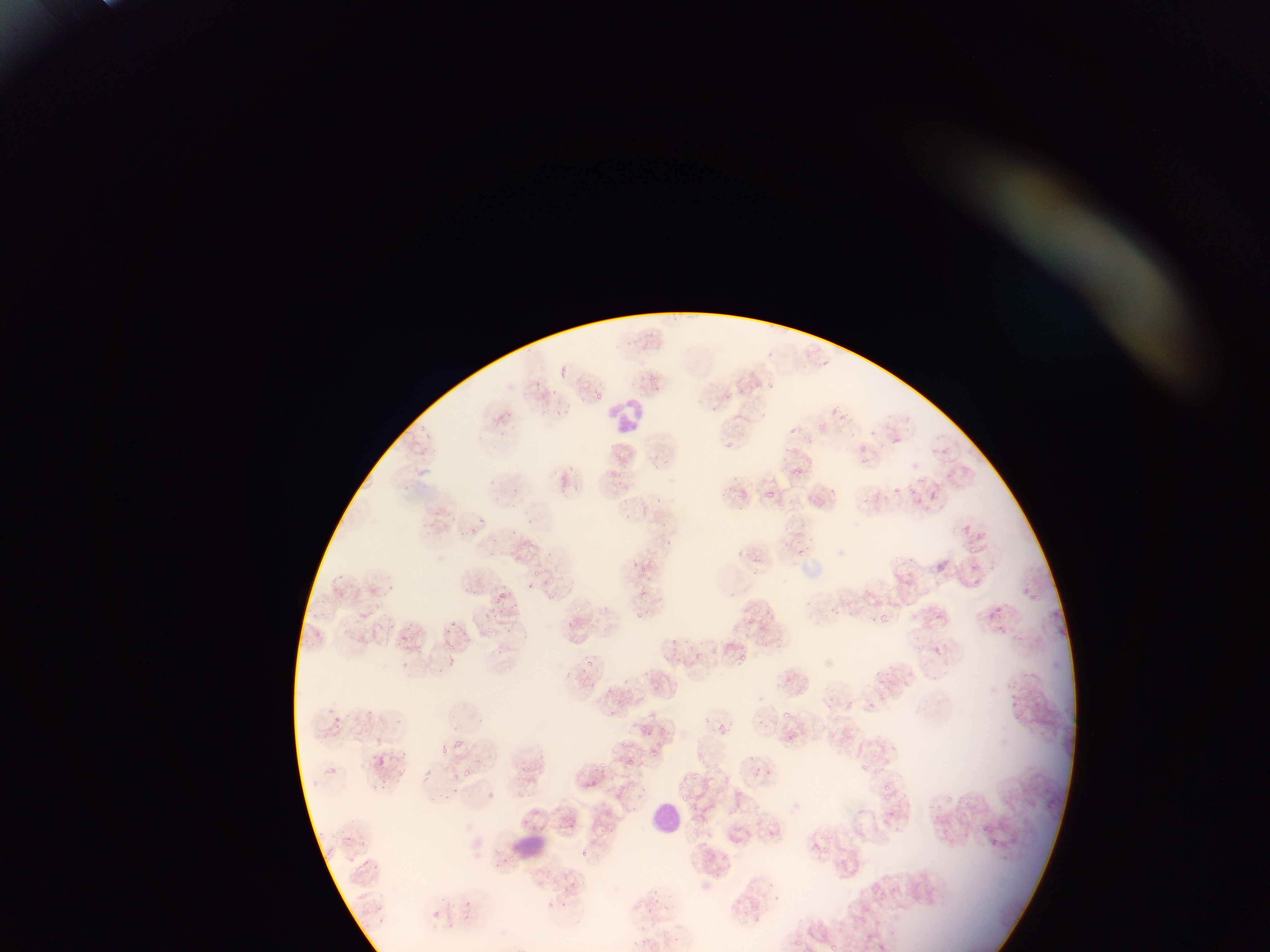
Plasmodium parasite locations = approximate bounding boxes as {left, top, right, bottom} in pixels: {639, 372, 656, 386}, {580, 387, 597, 407}, {543, 388, 570, 408}, {831, 407, 840, 415}, {553, 408, 571, 422}, {864, 423, 874, 436}, {788, 427, 798, 435}, {892, 434, 910, 453}, {852, 450, 880, 472}, {789, 462, 808, 486}, {764, 477, 778, 505}, {614, 479, 624, 490}, {893, 481, 905, 501}, {928, 486, 940, 502}, {653, 495, 673, 511}, {617, 507, 632, 526}, {477, 514, 486, 524}, {505, 528, 517, 540}, {661, 533, 669, 549}, {793, 542, 806, 560}, {918, 551, 957, 575}, {631, 558, 645, 573}, {336, 571, 350, 579}, {528, 577, 540, 593}, {454, 583, 474, 595}, {1017, 585, 1041, 599}, {638, 586, 645, 596}, {498, 589, 511, 605}, {825, 602, 837, 617}, {989, 605, 1005, 619}, {877, 609, 902, 623}, {631, 610, 654, 629}, {443, 615, 451, 625}, {738, 615, 752, 633}, {564, 618, 574, 630}, {436, 628, 448, 642}, {670, 636, 678, 642}, {727, 637, 747, 670}, {933, 647, 945, 655}, {447, 650, 457, 666}, {695, 650, 703, 670}, {587, 660, 594, 672}, {622, 675, 629, 687}, {864, 697, 876, 707}, {364, 702, 372, 712}, {320, 707, 342, 725}, {751, 715, 767, 734}, {640, 718, 655, 735}, {719, 718, 731, 735}, {372, 735, 386, 749}, {439, 744, 448, 754}, {648, 747, 657, 759}, {370, 753, 389, 768}, {584, 753, 607, 780}, {625, 754, 638, 772}, {747, 754, 757, 762}, {863, 763, 877, 775}, {462, 767, 472, 776}, {884, 782, 895, 792}, {567, 814, 575, 823}, {979, 820, 992, 833}, {766, 821, 783, 856}, {811, 841, 821, 852}, {766, 889, 780, 907}, {464, 900, 472, 907} | approximate {x, y} pixel centers of objects too small to bound: {823, 361}, {531, 520}
leukocyte locations = approximate bounding boxes as {left, top, right, bottom} in pixels: {615, 402, 644, 432}, {651, 797, 688, 832}, {514, 823, 547, 859}
preparation = thin blood smear
capture = mobile-phone photograph through a microscope
field of view = single
country = Ghana
image size = 1270×952 pixels